Report the malaria status of this cell.
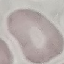

Uninfected.

capture = smartphone through the microscope eyepiece
stain = Giemsa
image type = automatically extracted cell patch, resized to 64 × 64 pixels
preparation = thin smear